Classify this cell by malaria status.
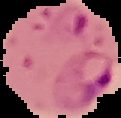
Parasitized.

image_type: segmented cell region on a black background
image_size: 121×118 pixels
preparation: thin blood smear